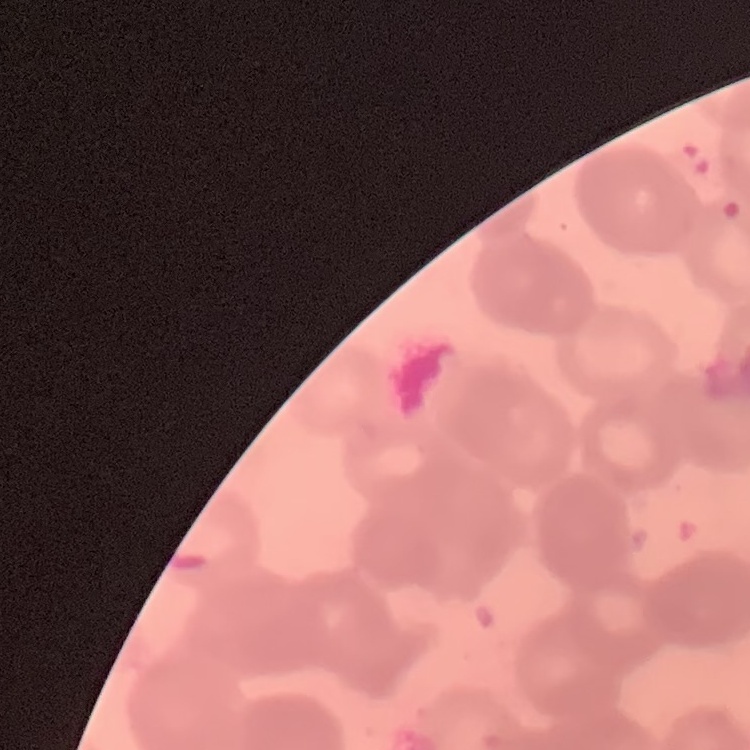
Summary:
  - Red blood cell morphology: rouleaux formation
  - Stain: Field's or Giemsa
  - Image type: one tile cut from a larger photomicrograph
  - Preparation: thin blood smear